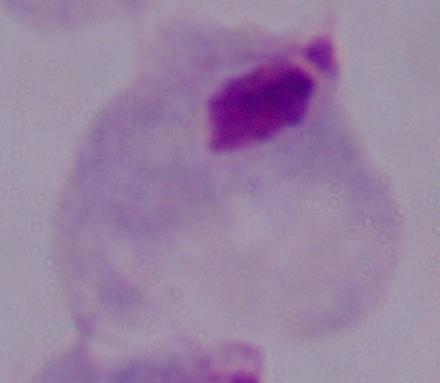
Captured at 1000x magnification. Photomicrograph. A trichomonad is seen.